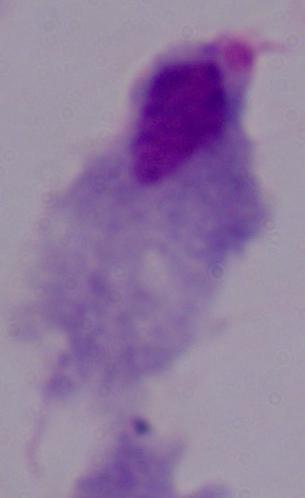 Micrograph. A trichomonad is seen. Captured at 1000x magnification.